Classify this cell by malaria status.
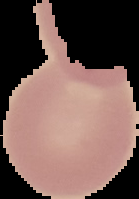

Uninfected.

Cell region segmented out of the field of view; the surrounding area is masked to black. Image is 139×199 pixels. From a thin blood film.